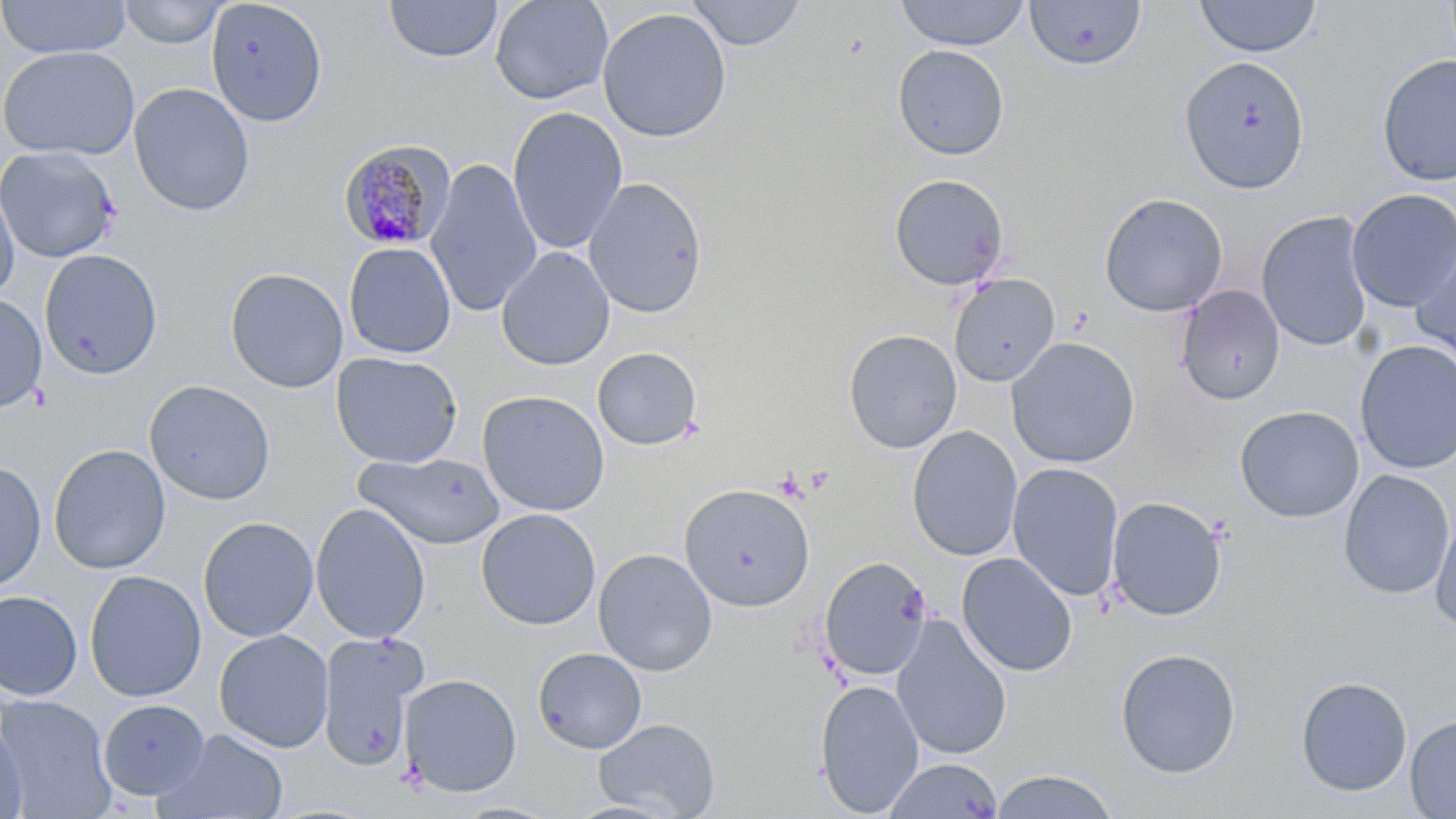

slide-level diagnosis = Plasmodium malariae
preparation = thin blood film
Plasmodium malariae-infected red blood cell locations = approximate bounding boxes as (x1, y1, x2, y2) in pixels: (337, 138, 458, 251)
modality = light microscopy
image size = 1456×819 pixels
field of view = one of a larger specimen
uninfected red blood cell locations = approximate bounding boxes as (x1, y1, x2, y2) in pixels: (0, 0, 131, 59), (205, 0, 328, 127), (384, 0, 502, 63), (489, 0, 614, 105), (686, 0, 808, 50), (893, 0, 1032, 50), (1192, 0, 1323, 58), (118, 1, 228, 48), (1024, 1, 1147, 72), (597, 7, 732, 142), (1, 45, 140, 160), (892, 45, 1010, 161), (1376, 54, 1456, 187), (1178, 55, 1310, 193), (128, 83, 255, 217), (507, 107, 628, 254), (0, 145, 122, 264), (426, 157, 543, 318), (888, 173, 1011, 291), (583, 176, 708, 319), (0, 177, 19, 303), (1345, 188, 1456, 311), (1098, 192, 1228, 317), (1256, 210, 1373, 352), (1411, 234, 1456, 364), (344, 242, 457, 359), (497, 246, 615, 371), (39, 250, 163, 380), (225, 267, 348, 393), (948, 273, 1061, 387), (1176, 285, 1285, 405), (0, 292, 48, 413), (843, 329, 962, 453), (1006, 336, 1141, 469), (1354, 340, 1456, 474), (592, 346, 703, 450), (330, 351, 463, 468), (144, 379, 276, 506), (476, 389, 611, 517), (1234, 405, 1364, 523), (906, 426, 1023, 561), (48, 444, 171, 575), (353, 451, 506, 550), (0, 460, 46, 594), (1007, 462, 1124, 601), (1338, 470, 1454, 600), (678, 482, 816, 612), (1106, 496, 1228, 621), (310, 503, 430, 643), (476, 508, 601, 630), (1429, 509, 1456, 633), (198, 516, 319, 642), (593, 548, 717, 676), (956, 552, 1077, 677), (818, 555, 933, 681), (84, 570, 206, 703), (0, 590, 83, 701), (892, 616, 1012, 760), (214, 629, 334, 753), (317, 633, 425, 772), (533, 647, 647, 753), (1115, 648, 1241, 779), (399, 673, 522, 798), (1295, 676, 1413, 797), (814, 679, 924, 816), (0, 694, 116, 817), (98, 698, 209, 800), (1404, 714, 1456, 818), (593, 718, 721, 818), (0, 722, 28, 819), (158, 728, 289, 818), (883, 757, 1003, 818), (988, 769, 1121, 819)
stain = May-Grünwald-Giemsa
magnification = 1000x